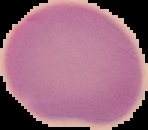
{
  "preparation": "thin blood film",
  "image_size": "148×130 pixels",
  "malaria_status": "uninfected",
  "image_type": "cell region segmented out of the field of view; surrounding area masked to black"
}